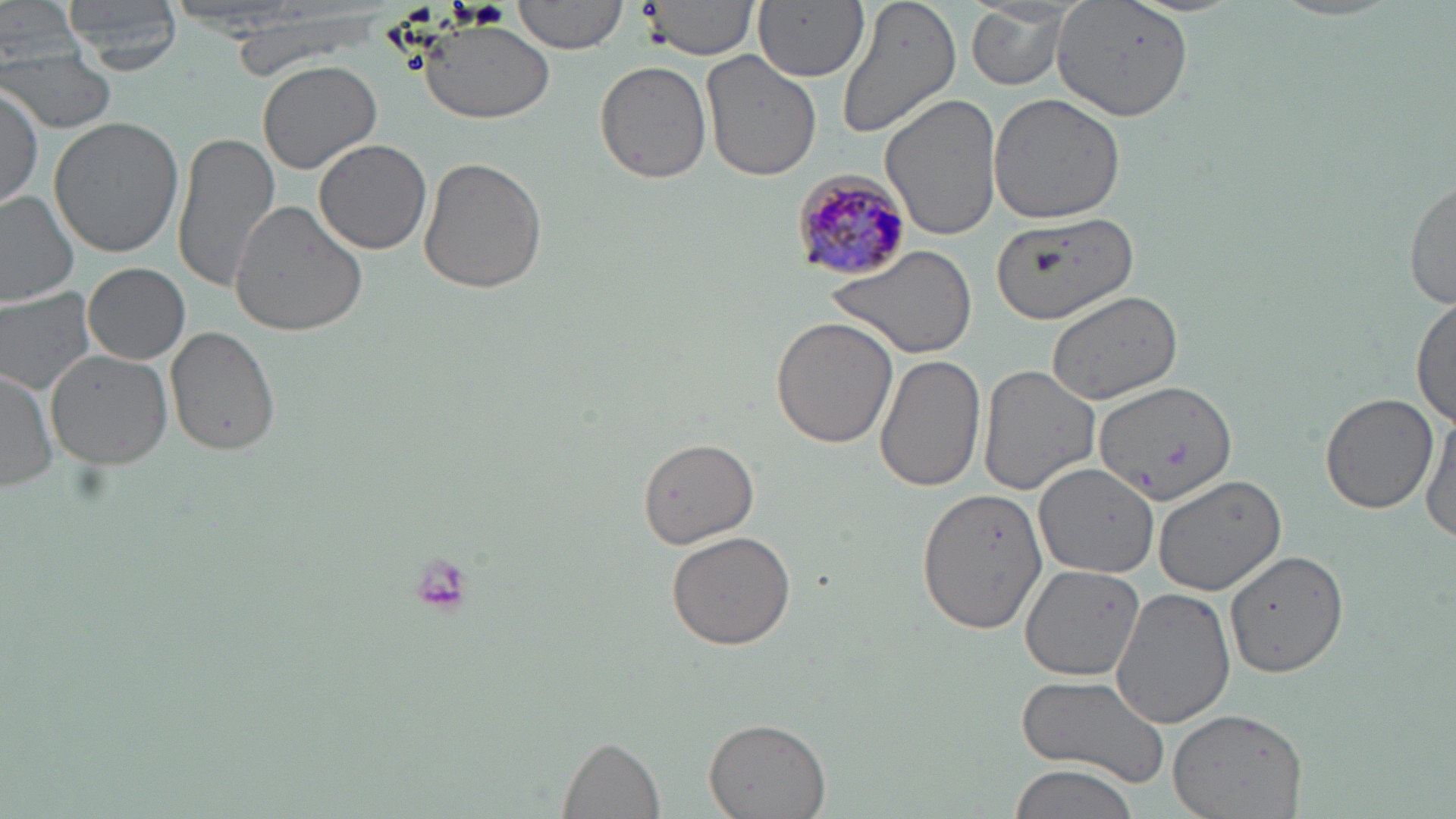

slide-level diagnosis = Plasmodium malariae
modality = optical microscopy
preparation = thin blood smear
uninfected red blood cell locations = approximate bounding boxes as (x1, y1, x2, y2) in pixels: (3, 0, 83, 60), (61, 0, 186, 72), (515, 0, 628, 54), (638, 0, 760, 59), (754, 0, 867, 82), (837, 0, 961, 141), (1053, 0, 1190, 122), (965, 3, 1076, 90), (421, 18, 553, 121), (2, 49, 116, 135), (701, 50, 822, 184), (257, 57, 383, 175), (595, 59, 713, 184), (1, 84, 45, 207), (881, 93, 1003, 241), (987, 94, 1127, 223), (50, 115, 188, 257), (172, 130, 281, 292), (314, 140, 432, 255), (417, 157, 548, 295), (1404, 177, 1456, 308), (0, 191, 79, 307), (231, 198, 370, 336), (990, 211, 1140, 323), (828, 243, 977, 359), (83, 263, 191, 364), (0, 288, 98, 398), (1045, 288, 1185, 403), (1412, 295, 1455, 428), (770, 317, 897, 448), (165, 327, 280, 458), (44, 347, 173, 472), (875, 354, 986, 493), (978, 363, 1101, 495), (0, 368, 59, 491), (1094, 380, 1238, 507), (1319, 391, 1439, 514), (1421, 408, 1456, 549), (637, 438, 759, 549), (1031, 464, 1161, 578), (1153, 474, 1286, 596), (916, 487, 1050, 638), (665, 531, 796, 651), (1225, 549, 1350, 680), (1020, 564, 1148, 680), (1110, 585, 1237, 730), (1017, 672, 1171, 786), (1168, 707, 1306, 818), (702, 717, 831, 818), (558, 736, 664, 816), (1003, 761, 1140, 819)
stain = May-Grünwald-Giemsa
Plasmodium malariae-infected red blood cell locations = approximate bounding boxes as (x1, y1, x2, y2) in pixels: (790, 170, 911, 282)
magnification = 1000x
image size = 1456×819 pixels
field of view = single